Identify the blood parasite species.
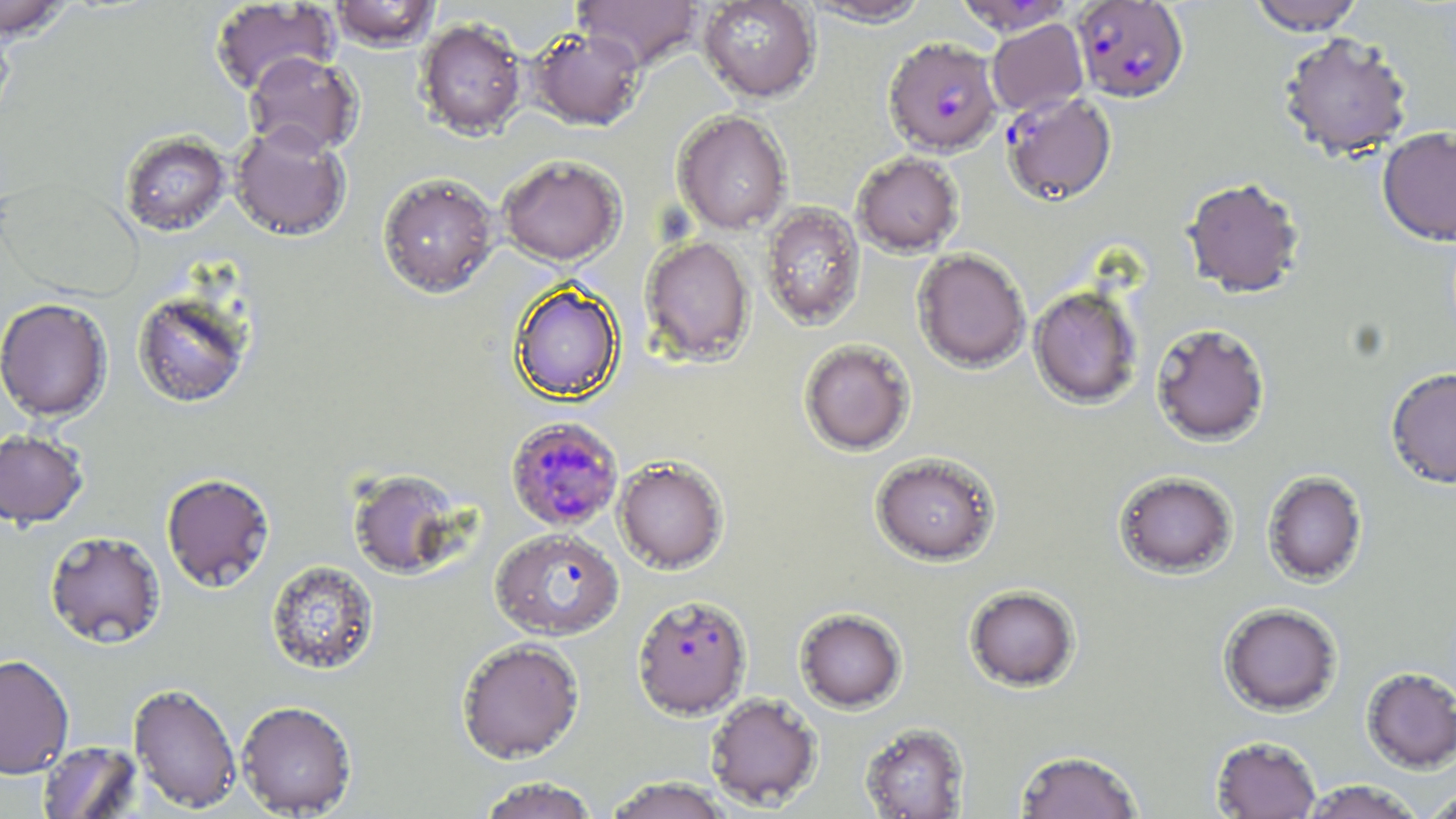
Plasmodium falciparum.

Approximate bounding boxes as named x1/y1/x2/y2 corners in pixels. Plasmodium falciparum-infected red blood cell locations: (x1=1071, y1=1, x2=1189, y2=103), (x1=883, y1=37, x2=1002, y2=156), (x1=1001, y1=92, x2=1117, y2=206), (x1=505, y1=416, x2=624, y2=532), (x1=490, y1=527, x2=624, y2=640), (x1=632, y1=593, x2=751, y2=719). Uninfected red blood cell locations: (x1=0, y1=0, x2=74, y2=40), (x1=574, y1=0, x2=703, y2=70), (x1=698, y1=0, x2=819, y2=103), (x1=800, y1=0, x2=932, y2=26), (x1=954, y1=0, x2=1077, y2=35), (x1=1247, y1=0, x2=1366, y2=35), (x1=209, y1=1, x2=339, y2=96), (x1=328, y1=1, x2=441, y2=51), (x1=0, y1=16, x2=16, y2=129), (x1=415, y1=17, x2=527, y2=139), (x1=986, y1=19, x2=1089, y2=116), (x1=529, y1=26, x2=646, y2=130), (x1=1278, y1=31, x2=1414, y2=160), (x1=243, y1=51, x2=363, y2=158), (x1=672, y1=110, x2=792, y2=235), (x1=229, y1=122, x2=351, y2=241), (x1=1377, y1=126, x2=1456, y2=246), (x1=120, y1=130, x2=231, y2=236), (x1=851, y1=151, x2=965, y2=257), (x1=497, y1=154, x2=626, y2=266), (x1=377, y1=171, x2=500, y2=298), (x1=0, y1=176, x2=143, y2=301), (x1=1181, y1=177, x2=1305, y2=299), (x1=759, y1=201, x2=866, y2=331), (x1=640, y1=235, x2=754, y2=366), (x1=912, y1=248, x2=1030, y2=373), (x1=510, y1=282, x2=624, y2=403), (x1=1028, y1=286, x2=1143, y2=408), (x1=131, y1=287, x2=255, y2=408), (x1=0, y1=297, x2=113, y2=422), (x1=1151, y1=323, x2=1271, y2=447), (x1=799, y1=339, x2=915, y2=455), (x1=1385, y1=367, x2=1456, y2=488), (x1=0, y1=428, x2=89, y2=528), (x1=870, y1=451, x2=1002, y2=566), (x1=613, y1=455, x2=729, y2=574), (x1=348, y1=468, x2=468, y2=579), (x1=1113, y1=471, x2=1238, y2=579), (x1=1262, y1=471, x2=1368, y2=587), (x1=161, y1=472, x2=275, y2=592), (x1=44, y1=530, x2=166, y2=648), (x1=265, y1=559, x2=381, y2=676), (x1=964, y1=585, x2=1081, y2=692), (x1=1218, y1=602, x2=1343, y2=716), (x1=795, y1=608, x2=907, y2=713), (x1=456, y1=637, x2=585, y2=763), (x1=0, y1=654, x2=74, y2=779), (x1=1361, y1=666, x2=1456, y2=773), (x1=129, y1=682, x2=242, y2=813), (x1=705, y1=692, x2=822, y2=810), (x1=235, y1=699, x2=357, y2=816), (x1=860, y1=722, x2=969, y2=818), (x1=1211, y1=736, x2=1321, y2=818), (x1=37, y1=741, x2=143, y2=818), (x1=1014, y1=749, x2=1144, y2=819), (x1=476, y1=776, x2=601, y2=819), (x1=603, y1=776, x2=735, y2=819), (x1=1299, y1=780, x2=1424, y2=818), (x1=1422, y1=789, x2=1456, y2=819). Image is 1456×819 pixels. Optical microscopy. Thin blood smear. One field of a larger specimen. 1000x magnification. May-Grünwald-Giemsa stain.